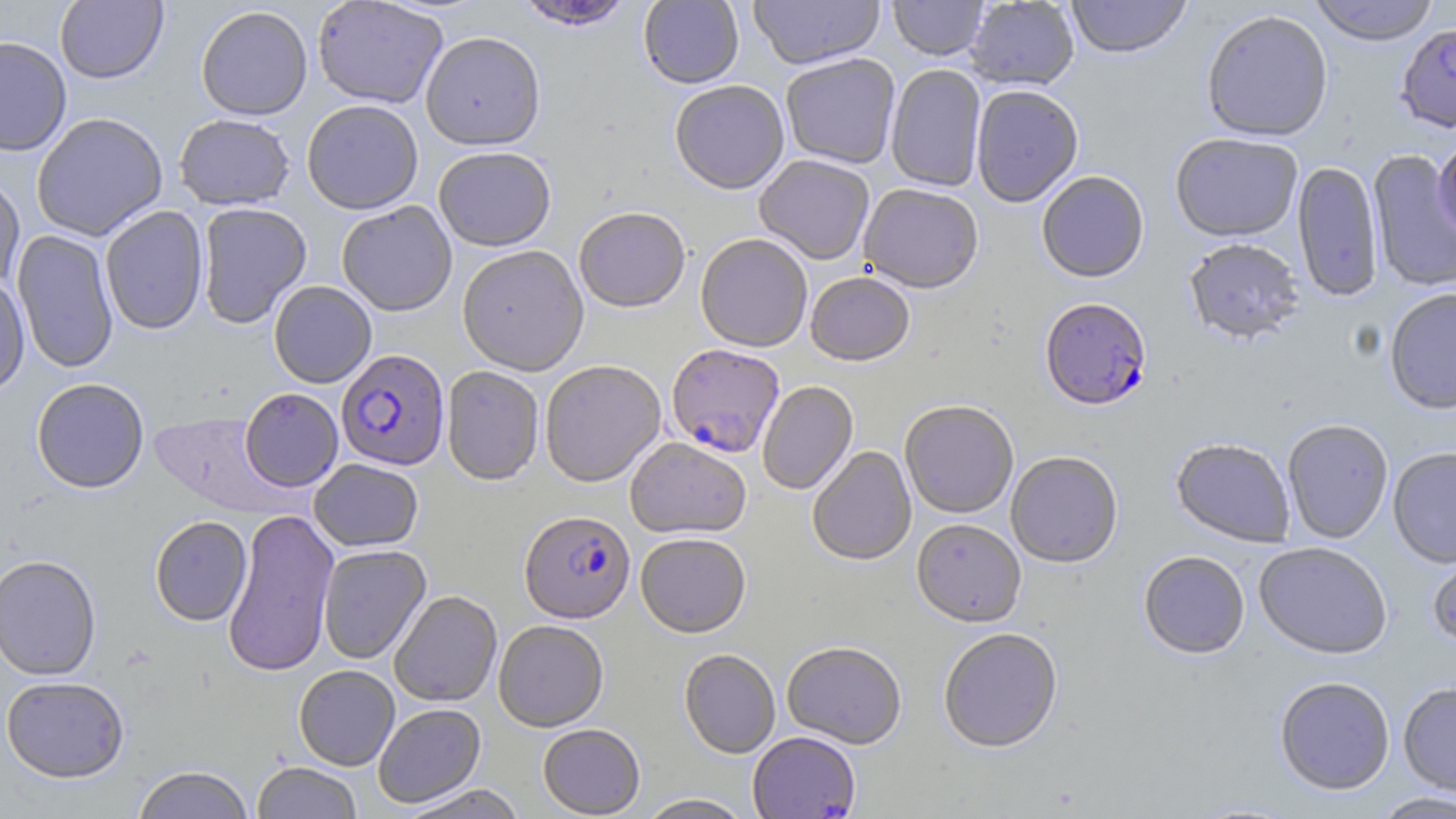
Approximate bounding boxes as named x1/y1/x2/y2 corners in pixels. Plasmodium falciparum-infected red blood cell locations: (x1=1040, y1=299, x2=1152, y2=412), (x1=666, y1=344, x2=784, y2=459), (x1=336, y1=349, x2=449, y2=470), (x1=519, y1=511, x2=635, y2=624). Uninfected red blood cell locations: (x1=514, y1=0, x2=634, y2=32), (x1=638, y1=0, x2=744, y2=89), (x1=748, y1=0, x2=885, y2=71), (x1=887, y1=0, x2=989, y2=61), (x1=1065, y1=0, x2=1192, y2=60), (x1=1308, y1=0, x2=1440, y2=46), (x1=55, y1=1, x2=168, y2=84), (x1=312, y1=1, x2=448, y2=109), (x1=965, y1=1, x2=1079, y2=91), (x1=195, y1=6, x2=313, y2=120), (x1=1201, y1=10, x2=1333, y2=143), (x1=1396, y1=23, x2=1456, y2=132), (x1=420, y1=31, x2=546, y2=151), (x1=0, y1=35, x2=72, y2=156), (x1=780, y1=54, x2=900, y2=170), (x1=886, y1=64, x2=987, y2=193), (x1=670, y1=82, x2=789, y2=196), (x1=971, y1=86, x2=1084, y2=208), (x1=302, y1=100, x2=423, y2=215), (x1=31, y1=112, x2=168, y2=241), (x1=174, y1=113, x2=295, y2=210), (x1=1170, y1=134, x2=1302, y2=243), (x1=1432, y1=137, x2=1456, y2=243), (x1=433, y1=148, x2=556, y2=252), (x1=1367, y1=150, x2=1456, y2=293), (x1=755, y1=156, x2=875, y2=266), (x1=1293, y1=161, x2=1383, y2=303), (x1=0, y1=171, x2=25, y2=292), (x1=1036, y1=172, x2=1149, y2=284), (x1=858, y1=185, x2=984, y2=296), (x1=197, y1=202, x2=311, y2=328), (x1=336, y1=202, x2=457, y2=316), (x1=100, y1=205, x2=209, y2=335), (x1=573, y1=209, x2=690, y2=314), (x1=12, y1=229, x2=119, y2=374), (x1=696, y1=235, x2=812, y2=353), (x1=1184, y1=239, x2=1304, y2=346), (x1=457, y1=246, x2=589, y2=377), (x1=805, y1=273, x2=915, y2=367), (x1=0, y1=274, x2=30, y2=397), (x1=269, y1=281, x2=377, y2=388), (x1=1384, y1=288, x2=1456, y2=415), (x1=540, y1=361, x2=666, y2=488), (x1=441, y1=366, x2=545, y2=486), (x1=31, y1=377, x2=150, y2=493), (x1=757, y1=381, x2=858, y2=496), (x1=240, y1=387, x2=344, y2=492), (x1=900, y1=401, x2=1018, y2=519), (x1=149, y1=410, x2=290, y2=517), (x1=1282, y1=420, x2=1394, y2=544), (x1=625, y1=437, x2=751, y2=540), (x1=1171, y1=439, x2=1295, y2=548), (x1=807, y1=446, x2=917, y2=566), (x1=1387, y1=447, x2=1456, y2=568), (x1=1006, y1=452, x2=1123, y2=568), (x1=308, y1=459, x2=424, y2=551), (x1=222, y1=508, x2=340, y2=677), (x1=150, y1=515, x2=252, y2=626), (x1=912, y1=519, x2=1026, y2=628), (x1=636, y1=534, x2=751, y2=639), (x1=1426, y1=541, x2=1456, y2=650), (x1=1254, y1=542, x2=1393, y2=659), (x1=318, y1=544, x2=431, y2=664), (x1=1139, y1=551, x2=1250, y2=660), (x1=0, y1=554, x2=102, y2=680), (x1=389, y1=591, x2=502, y2=707), (x1=493, y1=620, x2=609, y2=732), (x1=938, y1=629, x2=1064, y2=755), (x1=782, y1=642, x2=907, y2=749), (x1=679, y1=649, x2=781, y2=759), (x1=294, y1=665, x2=400, y2=770), (x1=1, y1=675, x2=130, y2=782), (x1=1274, y1=676, x2=1395, y2=796), (x1=1397, y1=682, x2=1456, y2=797), (x1=373, y1=703, x2=486, y2=808), (x1=537, y1=724, x2=645, y2=818), (x1=748, y1=732, x2=861, y2=819), (x1=252, y1=762, x2=362, y2=818), (x1=131, y1=765, x2=255, y2=819), (x1=398, y1=784, x2=528, y2=819), (x1=1371, y1=791, x2=1456, y2=818), (x1=637, y1=794, x2=754, y2=819). Slide-level diagnosis: Plasmodium falciparum. Light microscopy. Thin blood film. May-Grünwald-Giemsa-stained preparation. Single field of view. Image is 1456×819 pixels. Captured at 1000x magnification.